Locate and identify every blood parasite.
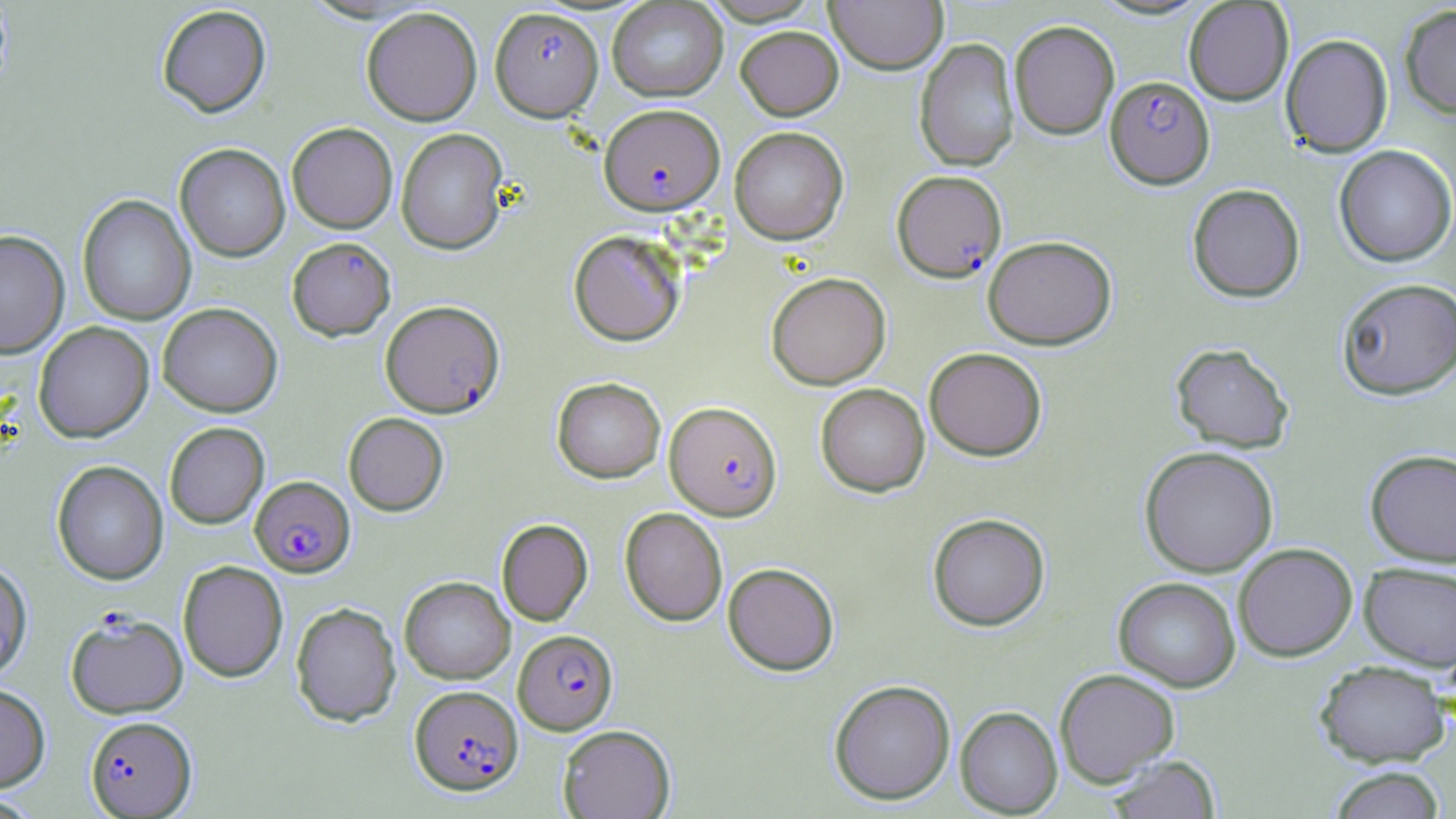
Approximate bounding boxes as [x1, y1, x2, y2] in pixels.
Plasmodium falciparum-infected red blood cells: [490, 7, 603, 120], [1105, 76, 1214, 189], [599, 103, 725, 214], [891, 169, 1006, 281], [380, 299, 505, 417], [664, 400, 782, 519], [250, 475, 355, 577], [65, 611, 188, 718], [513, 629, 618, 734], [410, 685, 522, 795], [85, 715, 197, 817].
No Plasmodium ovale, Plasmodium malariae, Plasmodium vivax, Babesia divergens, or Trypanosoma brucei observed.

Summary:
  - Uninfected red blood cell locations: [698, 0, 823, 25], [825, 0, 948, 74], [607, 1, 728, 102], [1183, 1, 1293, 106], [156, 4, 271, 117], [1399, 4, 1456, 119], [361, 6, 483, 126], [1009, 20, 1120, 140], [735, 26, 843, 120], [1280, 34, 1393, 157], [914, 38, 1020, 172], [287, 122, 398, 233], [730, 126, 848, 244], [396, 128, 509, 255], [175, 143, 290, 261], [1334, 144, 1456, 266], [1187, 183, 1305, 302], [77, 194, 196, 326], [569, 230, 685, 346], [0, 231, 70, 358], [982, 235, 1117, 349], [286, 237, 395, 340], [767, 272, 891, 389], [1337, 277, 1456, 400], [158, 303, 282, 417], [33, 321, 154, 442], [1170, 342, 1295, 453], [924, 347, 1047, 461], [552, 377, 665, 483], [815, 383, 930, 497], [343, 412, 449, 515], [164, 422, 269, 529], [1139, 446, 1278, 577], [1365, 448, 1456, 566], [52, 460, 168, 585], [620, 507, 727, 626], [927, 513, 1050, 631], [496, 519, 593, 625], [1233, 543, 1357, 661], [0, 559, 33, 683], [178, 560, 288, 682], [723, 562, 839, 676], [1359, 562, 1456, 670], [400, 576, 515, 684], [1113, 577, 1241, 692], [290, 601, 401, 726], [1314, 660, 1450, 767], [1054, 668, 1180, 787], [828, 679, 955, 805], [0, 683, 50, 792], [955, 706, 1062, 817], [557, 724, 676, 818], [1104, 755, 1223, 819], [1325, 766, 1447, 819]
  - Slide-level diagnosis: Plasmodium falciparum
  - Image size: 1456×819 pixels
  - Preparation: thin blood smear
  - Stain: May-Grünwald-Giemsa
  - Field of view: single
  - Modality: optical microscopy
  - Magnification: 1000x